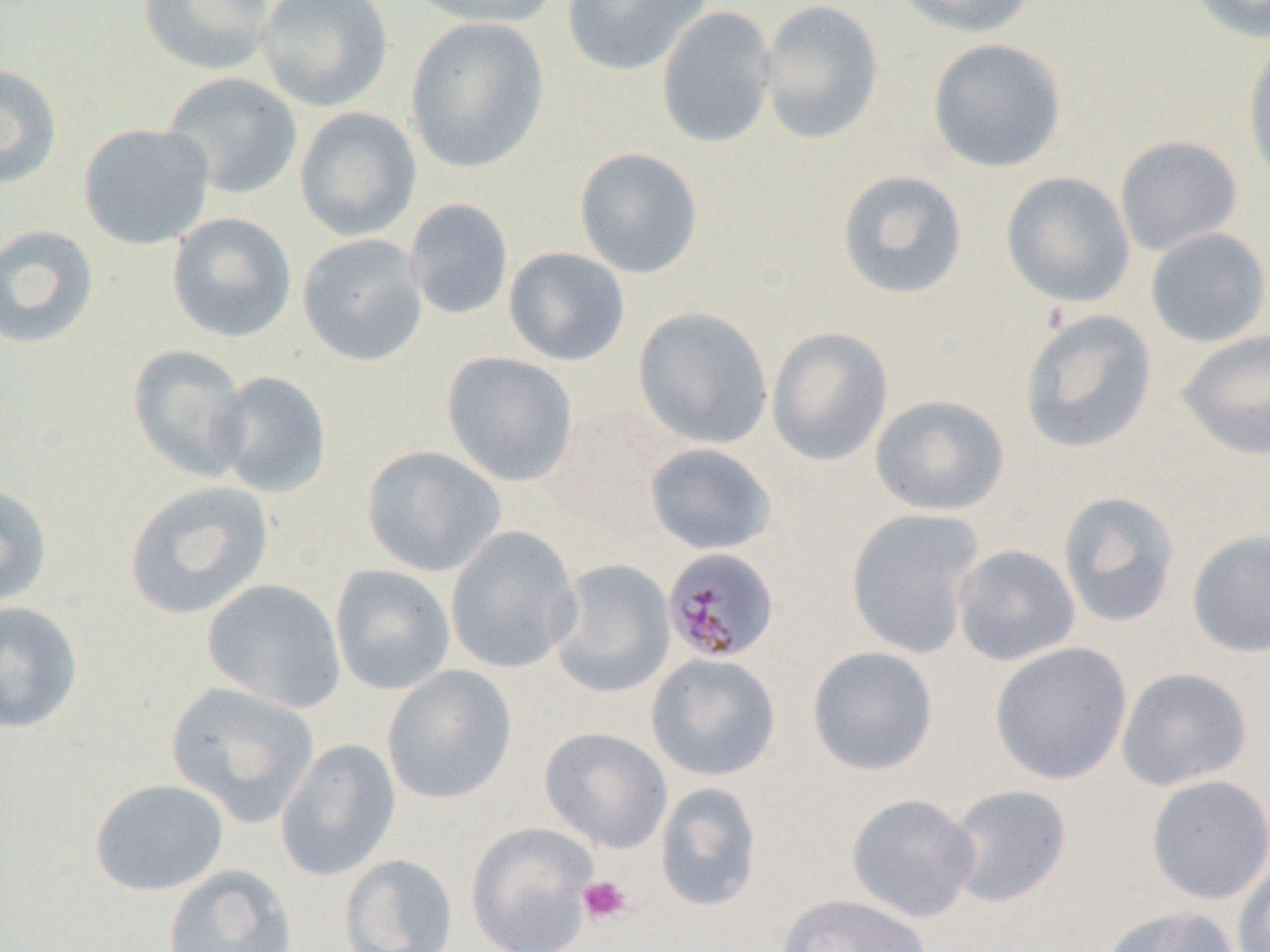

Approximate bounding boxes as named x1/y1/x2/y2 corners in pixels. Uninfected red blood cell locations: (x1=138, y1=0, x2=277, y2=76), (x1=256, y1=0, x2=393, y2=112), (x1=406, y1=0, x2=560, y2=29), (x1=560, y1=0, x2=713, y2=77), (x1=758, y1=0, x2=885, y2=146), (x1=895, y1=0, x2=1038, y2=39), (x1=1184, y1=0, x2=1270, y2=44), (x1=656, y1=6, x2=777, y2=150), (x1=405, y1=16, x2=551, y2=174), (x1=1241, y1=37, x2=1270, y2=197), (x1=927, y1=38, x2=1066, y2=172), (x1=0, y1=63, x2=63, y2=188), (x1=160, y1=72, x2=303, y2=200), (x1=294, y1=106, x2=422, y2=242), (x1=78, y1=122, x2=215, y2=250), (x1=1114, y1=135, x2=1242, y2=256), (x1=574, y1=147, x2=704, y2=279), (x1=836, y1=169, x2=969, y2=300), (x1=1001, y1=171, x2=1136, y2=308), (x1=404, y1=198, x2=514, y2=320), (x1=166, y1=212, x2=298, y2=343), (x1=0, y1=224, x2=99, y2=350), (x1=1144, y1=226, x2=1270, y2=348), (x1=297, y1=233, x2=428, y2=366), (x1=503, y1=246, x2=631, y2=367), (x1=633, y1=306, x2=773, y2=449), (x1=1018, y1=308, x2=1158, y2=455), (x1=767, y1=327, x2=894, y2=467), (x1=1176, y1=329, x2=1270, y2=460), (x1=128, y1=344, x2=251, y2=482), (x1=441, y1=351, x2=578, y2=487), (x1=210, y1=370, x2=332, y2=498), (x1=870, y1=394, x2=1010, y2=516), (x1=541, y1=401, x2=682, y2=539), (x1=644, y1=442, x2=778, y2=555), (x1=361, y1=445, x2=507, y2=577), (x1=123, y1=481, x2=274, y2=620), (x1=0, y1=482, x2=53, y2=608), (x1=1057, y1=490, x2=1182, y2=629), (x1=845, y1=507, x2=986, y2=659), (x1=445, y1=525, x2=581, y2=674), (x1=1186, y1=528, x2=1270, y2=658), (x1=952, y1=544, x2=1080, y2=666), (x1=548, y1=558, x2=676, y2=698), (x1=329, y1=563, x2=456, y2=696), (x1=202, y1=578, x2=347, y2=713), (x1=0, y1=600, x2=84, y2=735), (x1=988, y1=641, x2=1133, y2=785), (x1=806, y1=645, x2=939, y2=776), (x1=645, y1=653, x2=782, y2=782), (x1=382, y1=665, x2=517, y2=804), (x1=1116, y1=666, x2=1253, y2=791), (x1=165, y1=681, x2=320, y2=828), (x1=540, y1=727, x2=673, y2=853), (x1=275, y1=738, x2=401, y2=882), (x1=1145, y1=774, x2=1270, y2=905), (x1=89, y1=778, x2=229, y2=896), (x1=655, y1=781, x2=763, y2=912), (x1=943, y1=783, x2=1073, y2=908), (x1=846, y1=792, x2=980, y2=922), (x1=465, y1=821, x2=599, y2=952), (x1=339, y1=854, x2=459, y2=952), (x1=1232, y1=860, x2=1270, y2=952), (x1=162, y1=864, x2=298, y2=952), (x1=776, y1=893, x2=931, y2=952), (x1=1100, y1=904, x2=1241, y2=952). Platelet locations: (x1=578, y1=875, x2=633, y2=925). Plasmodium malariae-infected red blood cell locations: (x1=666, y1=554, x2=780, y2=660). Slide-level diagnosis: Plasmodium malariae. Captured at 1000x magnification. Image is 1270×952 pixels. One field of a larger specimen. Thin blood film. Light microscopy.